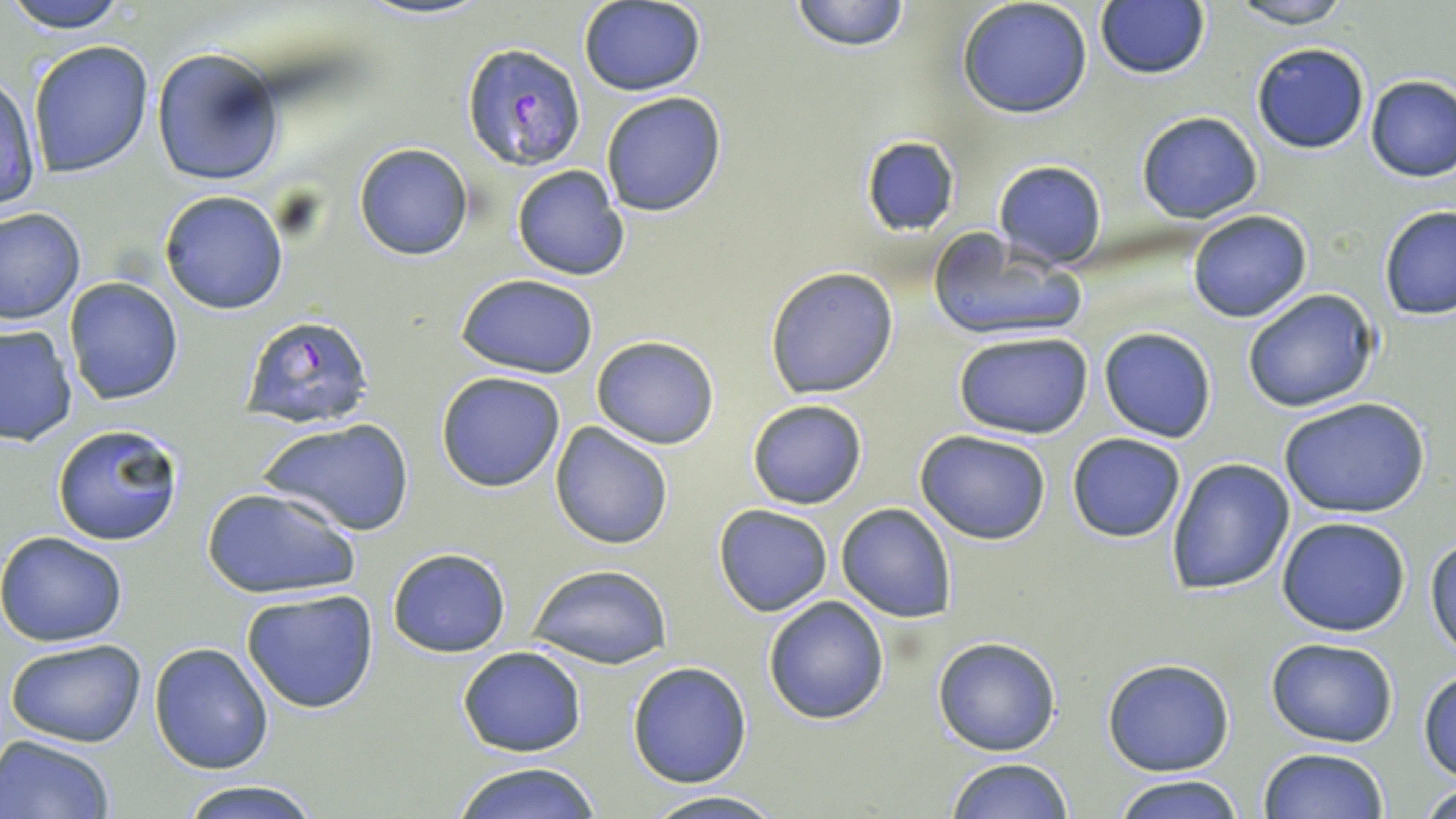 Approximate bounding boxes as named x1/y1/x2/y2 corners in pixels. Uninfected red blood cell locations: (x1=5, y1=0, x2=134, y2=31), (x1=789, y1=0, x2=911, y2=52), (x1=957, y1=0, x2=1094, y2=119), (x1=1229, y1=0, x2=1358, y2=27), (x1=578, y1=1, x2=706, y2=96), (x1=1095, y1=2, x2=1211, y2=80), (x1=28, y1=40, x2=155, y2=178), (x1=1250, y1=41, x2=1371, y2=154), (x1=151, y1=47, x2=284, y2=188), (x1=0, y1=73, x2=42, y2=212), (x1=1364, y1=73, x2=1456, y2=182), (x1=599, y1=91, x2=728, y2=217), (x1=1136, y1=111, x2=1263, y2=224), (x1=860, y1=136, x2=961, y2=236), (x1=353, y1=142, x2=474, y2=260), (x1=992, y1=160, x2=1107, y2=270), (x1=510, y1=165, x2=629, y2=281), (x1=158, y1=189, x2=290, y2=315), (x1=1379, y1=205, x2=1456, y2=322), (x1=0, y1=207, x2=85, y2=323), (x1=1188, y1=209, x2=1312, y2=323), (x1=928, y1=233, x2=1086, y2=344), (x1=764, y1=266, x2=899, y2=398), (x1=457, y1=275, x2=600, y2=377), (x1=64, y1=277, x2=183, y2=404), (x1=1241, y1=288, x2=1379, y2=413), (x1=0, y1=324, x2=76, y2=447), (x1=1099, y1=327, x2=1217, y2=443), (x1=953, y1=331, x2=1095, y2=440), (x1=590, y1=335, x2=719, y2=449), (x1=435, y1=371, x2=567, y2=493), (x1=1278, y1=397, x2=1430, y2=520), (x1=746, y1=398, x2=870, y2=511), (x1=260, y1=418, x2=413, y2=537), (x1=52, y1=420, x2=185, y2=547), (x1=550, y1=422, x2=674, y2=551), (x1=915, y1=428, x2=1052, y2=545), (x1=1066, y1=431, x2=1187, y2=543), (x1=1165, y1=457, x2=1297, y2=594), (x1=202, y1=486, x2=358, y2=600), (x1=836, y1=502, x2=957, y2=621), (x1=714, y1=504, x2=834, y2=616), (x1=1277, y1=516, x2=1413, y2=638), (x1=0, y1=531, x2=127, y2=645), (x1=1425, y1=533, x2=1456, y2=660), (x1=386, y1=547, x2=511, y2=658), (x1=528, y1=564, x2=674, y2=670), (x1=241, y1=589, x2=381, y2=715), (x1=763, y1=596, x2=889, y2=724), (x1=933, y1=637, x2=1060, y2=755), (x1=5, y1=638, x2=148, y2=749), (x1=1265, y1=638, x2=1399, y2=747), (x1=149, y1=642, x2=273, y2=773), (x1=457, y1=646, x2=587, y2=757), (x1=1101, y1=657, x2=1235, y2=775), (x1=627, y1=661, x2=752, y2=788), (x1=1419, y1=667, x2=1456, y2=780), (x1=0, y1=733, x2=114, y2=819), (x1=1259, y1=748, x2=1389, y2=819), (x1=946, y1=757, x2=1077, y2=818), (x1=450, y1=762, x2=605, y2=819), (x1=1113, y1=774, x2=1246, y2=819), (x1=1417, y1=778, x2=1455, y2=817), (x1=176, y1=779, x2=324, y2=818), (x1=639, y1=792, x2=790, y2=819). Plasmodium falciparum-infected red blood cell locations: (x1=461, y1=42, x2=586, y2=171), (x1=241, y1=316, x2=372, y2=428). Slide-level diagnosis: Plasmodium falciparum. Captured at 1000x magnification. Thin blood smear. One field of a larger specimen. Light microscopy. May-Grünwald-Giemsa-stained preparation. Image is 1456×819 pixels.